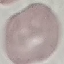

Summary:
  - Malaria status: uninfected
  - Capture: smartphone through the microscope eyepiece
  - Preparation: thin smear
  - Image type: automatically extracted cell patch, resized to 64 × 64 pixels
  - Stain: Giemsa